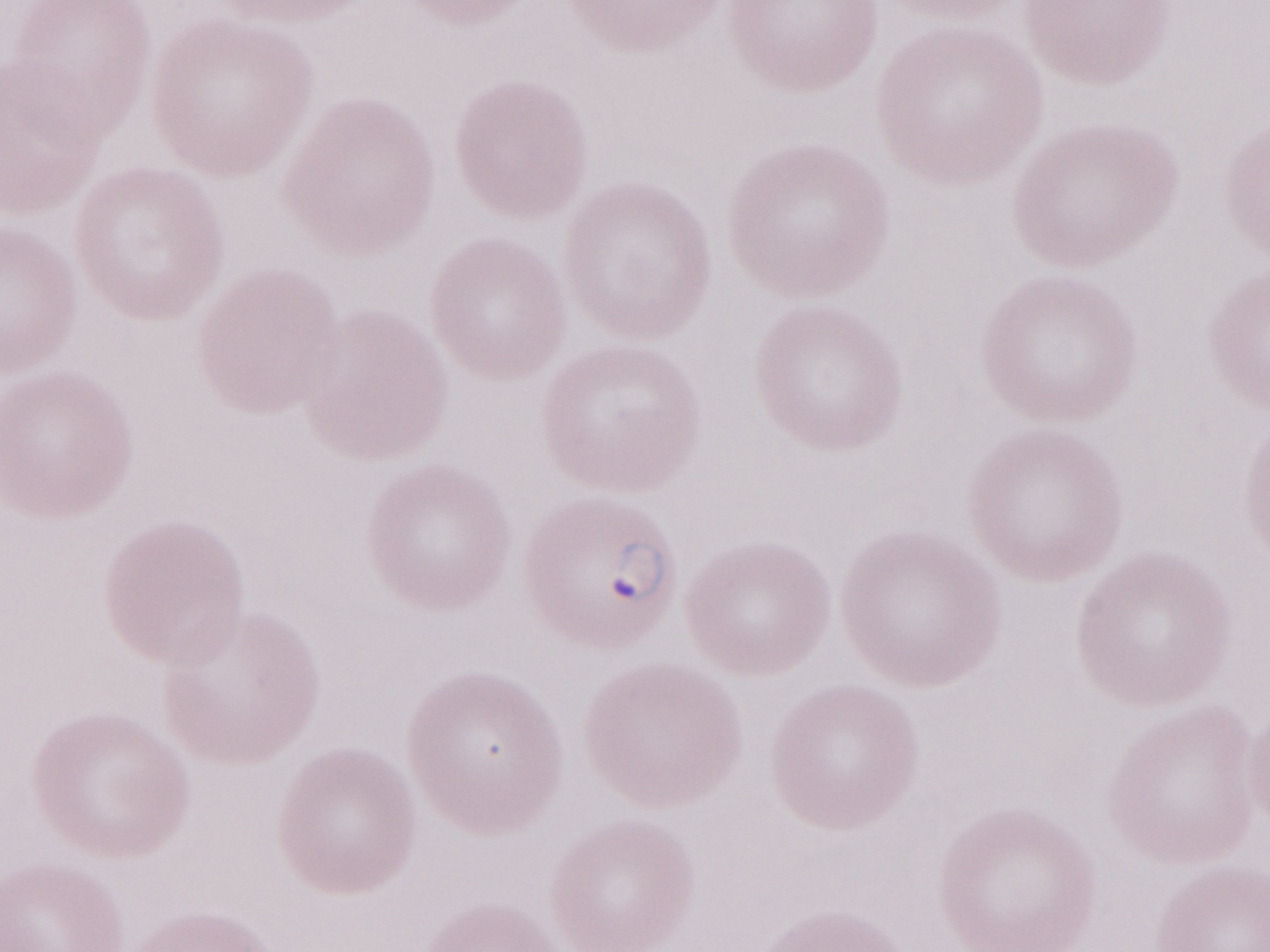 May-Grünwald-Giemsa stain. Thin peripheral-blood smear. 1,000x magnification. Malaria diagnosis (patient-level): positive. One field of this slide. Olympus BX43 microscope and DP73 digital camera. Image is 1270×952 pixels.